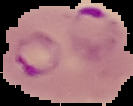

image_size: 133×106 pixels
result: Plasmodium parasites identified
preparation: thin blood smear
image_type: segmented cell region on a black background